Name the cell type shown.
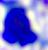
This is a leukocyte.

modality = micrograph
magnification = 400x